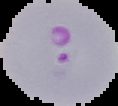 Image is 118×106 pixels. From a thin blood smear. Result: Plasmodium parasites identified. The area outside the segmented cell region is set to black.